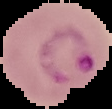

Summary:
  - Image type: segmented cell region with the area outside set to black
  - Image size: 112×109 pixels
  - Preparation: thin blood smear
  - Malaria status: parasitized